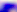
{
  "modality": "photomicrograph",
  "magnification": "400x",
  "identification": "Toxoplasma gondii"
}